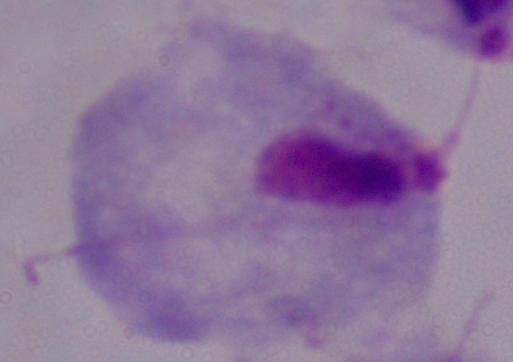

{
  "modality": "photomicrograph",
  "magnification": "1000x",
  "identification": "trichomonad"
}